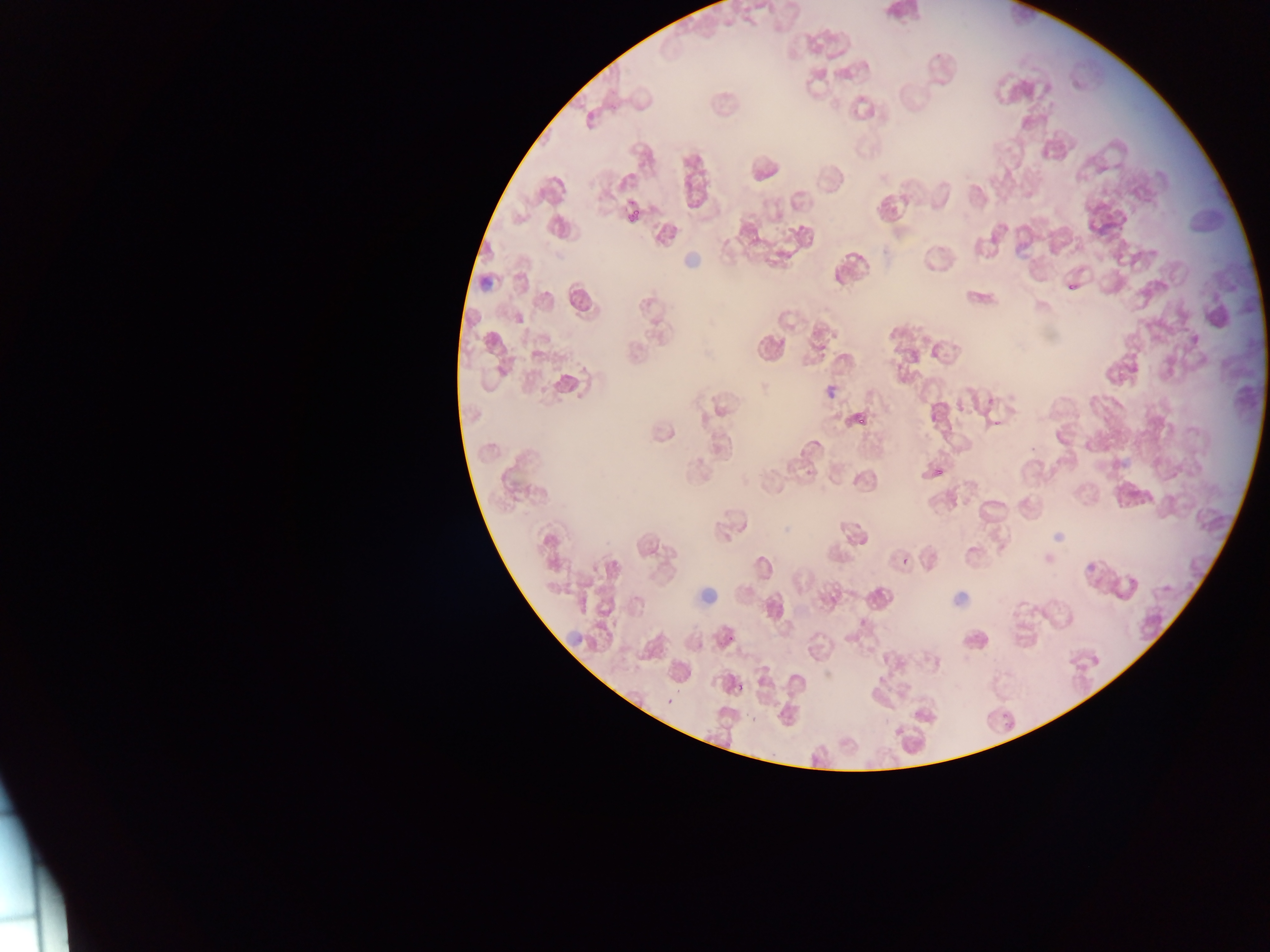
Approximate bounding boxes as (left, top, right, bottom) in pixels.
Summary:
  - Malaria parasite locations: (623, 199, 653, 222), (1067, 282, 1076, 290), (985, 396, 996, 408), (854, 412, 868, 424), (933, 463, 948, 476), (904, 555, 911, 563), (1118, 577, 1141, 600), (725, 634, 734, 642), (735, 683, 745, 693), (666, 698, 675, 706), (752, 713, 760, 722), (1006, 722, 1014, 730) | approximate (x, y) pixel centers of objects too small to bound: (995, 424), (905, 560), (701, 646)
  - Country: Ghana
  - Field of view: single
  - Preparation: thin blood smear
  - Image size: 1270×952 pixels
  - Capture: mobile-phone photograph through a microscope